Comment on the morphology of the erythrocytes.
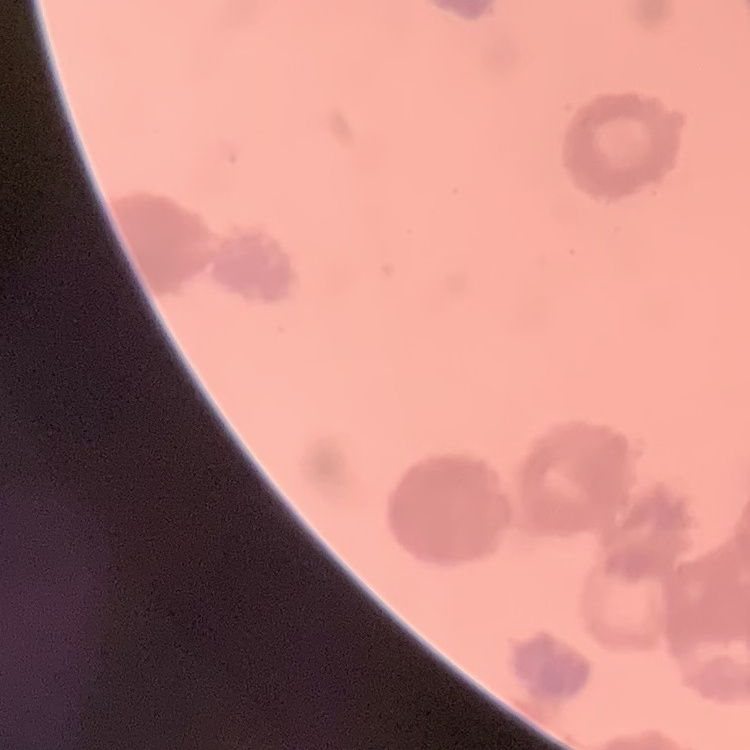

They show rouleaux formation.

Thin blood film. One tile cut from a larger photomicrograph. Stained with either Field's or Giemsa.